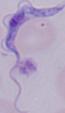

Summary:
  - Magnification: 1000x
  - Modality: micrograph
  - Identification: trypanosome